Locate every blood parasite and identify its species.
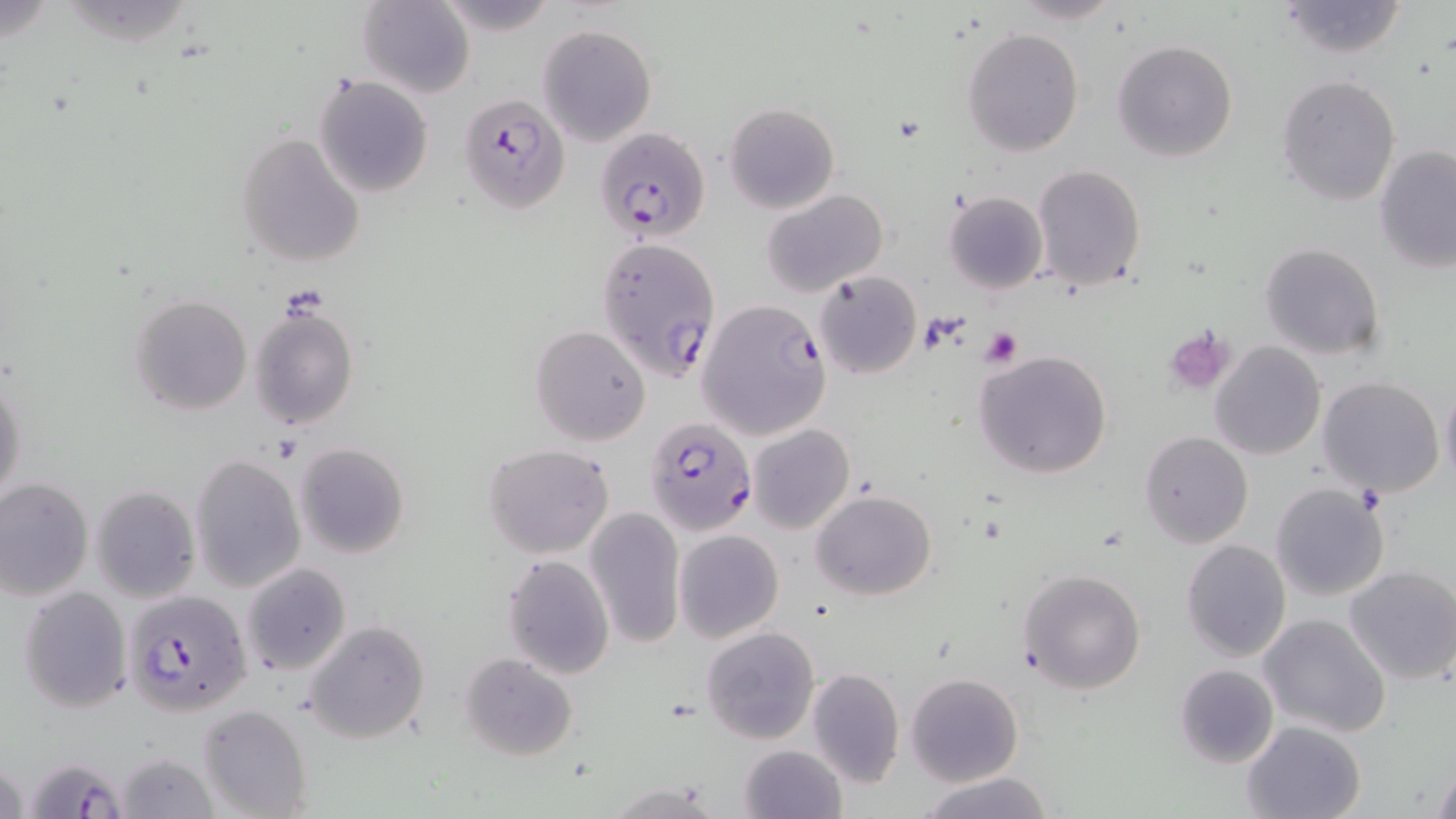
Approximate bounding boxes as named x1/y1/x2/y2 corners in pixels.
Plasmodium falciparum-infected red blood cells: (x1=456, y1=90, x2=571, y2=214), (x1=594, y1=126, x2=711, y2=244), (x1=597, y1=236, x2=721, y2=382), (x1=697, y1=298, x2=832, y2=441), (x1=650, y1=426, x2=759, y2=531), (x1=122, y1=589, x2=252, y2=717), (x1=25, y1=761, x2=130, y2=819).
No Plasmodium ovale, Plasmodium malariae, Plasmodium vivax, Babesia divergens, or Trypanosoma brucei observed.

slide-level diagnosis = Plasmodium falciparum
preparation = thin blood film
stain = May-Grünwald-Giemsa
modality = optical microscopy
platelet locations = approximate bounding boxes as named x1/y1/x2/y2 corners in pixels: (x1=979, y1=326, x2=1023, y2=368), (x1=1164, y1=326, x2=1236, y2=396)
field of view = single
magnification = 1000x
image size = 1456×819 pixels
uninfected red blood cell locations = approximate bounding boxes as named x1/y1/x2/y2 corners in pixels: (x1=1008, y1=0, x2=1125, y2=25), (x1=1273, y1=0, x2=1410, y2=59), (x1=357, y1=1, x2=475, y2=97), (x1=538, y1=24, x2=657, y2=146), (x1=962, y1=27, x2=1083, y2=156), (x1=1111, y1=39, x2=1238, y2=164), (x1=315, y1=75, x2=435, y2=198), (x1=1277, y1=75, x2=1402, y2=207), (x1=725, y1=102, x2=839, y2=212), (x1=236, y1=134, x2=366, y2=267), (x1=1374, y1=145, x2=1455, y2=275), (x1=1032, y1=164, x2=1147, y2=291), (x1=761, y1=188, x2=889, y2=295), (x1=942, y1=191, x2=1048, y2=295), (x1=1259, y1=242, x2=1386, y2=361), (x1=812, y1=271, x2=922, y2=379), (x1=130, y1=294, x2=252, y2=416), (x1=249, y1=301, x2=359, y2=430), (x1=529, y1=325, x2=651, y2=445), (x1=1210, y1=341, x2=1326, y2=460), (x1=973, y1=350, x2=1113, y2=478), (x1=0, y1=371, x2=27, y2=508), (x1=1317, y1=376, x2=1446, y2=499), (x1=1439, y1=381, x2=1456, y2=486), (x1=748, y1=423, x2=856, y2=535), (x1=1139, y1=431, x2=1253, y2=548), (x1=295, y1=442, x2=410, y2=560), (x1=483, y1=443, x2=614, y2=558), (x1=190, y1=454, x2=306, y2=592), (x1=0, y1=477, x2=93, y2=601), (x1=1270, y1=483, x2=1391, y2=602), (x1=92, y1=485, x2=200, y2=602), (x1=812, y1=491, x2=937, y2=600), (x1=584, y1=506, x2=686, y2=650), (x1=674, y1=530, x2=784, y2=644), (x1=1179, y1=539, x2=1291, y2=662), (x1=502, y1=553, x2=615, y2=678), (x1=242, y1=562, x2=352, y2=676), (x1=1345, y1=566, x2=1456, y2=686), (x1=1017, y1=568, x2=1147, y2=695), (x1=18, y1=585, x2=133, y2=713), (x1=1258, y1=613, x2=1390, y2=738), (x1=306, y1=620, x2=430, y2=744), (x1=700, y1=626, x2=819, y2=745), (x1=459, y1=652, x2=578, y2=763), (x1=1173, y1=663, x2=1278, y2=769), (x1=806, y1=667, x2=905, y2=787), (x1=905, y1=673, x2=1024, y2=787), (x1=199, y1=704, x2=311, y2=818), (x1=1241, y1=720, x2=1367, y2=818), (x1=738, y1=744, x2=846, y2=819), (x1=117, y1=750, x2=219, y2=819), (x1=1430, y1=760, x2=1456, y2=817), (x1=919, y1=771, x2=1055, y2=819), (x1=605, y1=782, x2=724, y2=818)